Identify the parasite.
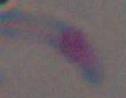

This is Toxoplasma gondii.

Micrograph. Captured at 1000x magnification.